State the blood parasite species.
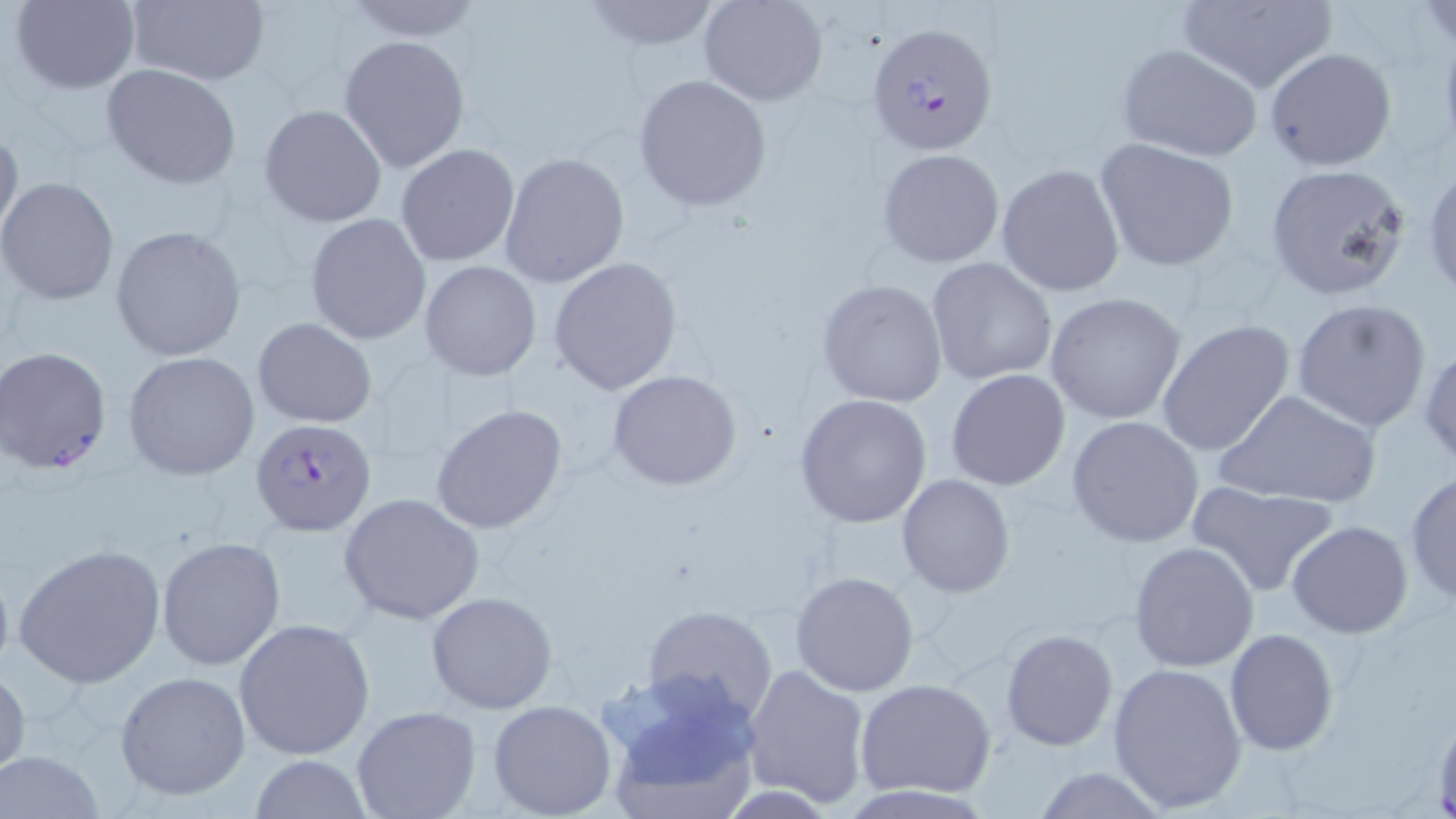

Plasmodium falciparum.

Approximate bounding boxes as named x1/y1/x2/y2 corners in pixels. Uninfected red blood cell locations: (x1=9, y1=0, x2=141, y2=95), (x1=577, y1=0, x2=721, y2=50), (x1=697, y1=0, x2=829, y2=107), (x1=1174, y1=0, x2=1338, y2=93), (x1=123, y1=1, x2=270, y2=86), (x1=1419, y1=1, x2=1456, y2=55), (x1=341, y1=2, x2=487, y2=43), (x1=339, y1=35, x2=472, y2=175), (x1=1116, y1=44, x2=1264, y2=163), (x1=1265, y1=47, x2=1397, y2=171), (x1=101, y1=64, x2=242, y2=189), (x1=632, y1=74, x2=772, y2=212), (x1=258, y1=104, x2=388, y2=229), (x1=0, y1=121, x2=23, y2=247), (x1=1094, y1=137, x2=1240, y2=273), (x1=395, y1=143, x2=521, y2=269), (x1=878, y1=149, x2=1005, y2=267), (x1=499, y1=152, x2=631, y2=289), (x1=1423, y1=161, x2=1456, y2=305), (x1=1263, y1=162, x2=1414, y2=302), (x1=995, y1=163, x2=1126, y2=299), (x1=1, y1=177, x2=120, y2=305), (x1=305, y1=213, x2=432, y2=345), (x1=110, y1=225, x2=248, y2=363), (x1=549, y1=257, x2=683, y2=396), (x1=925, y1=258, x2=1058, y2=388), (x1=420, y1=260, x2=542, y2=382), (x1=817, y1=278, x2=948, y2=408), (x1=1045, y1=293, x2=1187, y2=425), (x1=1291, y1=298, x2=1433, y2=433), (x1=252, y1=318, x2=376, y2=427), (x1=1156, y1=319, x2=1296, y2=456), (x1=1420, y1=343, x2=1456, y2=472), (x1=122, y1=350, x2=260, y2=481), (x1=607, y1=369, x2=743, y2=491), (x1=946, y1=369, x2=1071, y2=492), (x1=1211, y1=388, x2=1382, y2=510), (x1=794, y1=394, x2=933, y2=527), (x1=430, y1=403, x2=569, y2=535), (x1=1066, y1=415, x2=1205, y2=548), (x1=1403, y1=470, x2=1456, y2=606), (x1=896, y1=474, x2=1016, y2=597), (x1=1186, y1=481, x2=1339, y2=597), (x1=338, y1=492, x2=485, y2=625), (x1=1287, y1=521, x2=1413, y2=639), (x1=156, y1=535, x2=287, y2=671), (x1=1129, y1=540, x2=1260, y2=671), (x1=13, y1=542, x2=168, y2=691), (x1=791, y1=570, x2=920, y2=697), (x1=427, y1=591, x2=560, y2=714), (x1=640, y1=606, x2=777, y2=725), (x1=233, y1=618, x2=375, y2=761), (x1=1001, y1=628, x2=1117, y2=750), (x1=1224, y1=629, x2=1339, y2=755), (x1=742, y1=662, x2=872, y2=808), (x1=1105, y1=663, x2=1249, y2=813), (x1=0, y1=665, x2=29, y2=778), (x1=114, y1=671, x2=252, y2=802), (x1=595, y1=673, x2=767, y2=813), (x1=855, y1=677, x2=996, y2=800), (x1=486, y1=699, x2=617, y2=818), (x1=352, y1=707, x2=480, y2=819), (x1=0, y1=749, x2=107, y2=819), (x1=249, y1=753, x2=373, y2=819), (x1=1028, y1=766, x2=1173, y2=818). Plasmodium falciparum-infected red blood cell locations: (x1=868, y1=22, x2=999, y2=157), (x1=0, y1=347, x2=113, y2=473), (x1=252, y1=417, x2=378, y2=537). Thin blood smear. One field of a larger specimen. Light microscopy. 1000x magnification. Image is 1456×819 pixels. May-Grünwald-Giemsa stain.